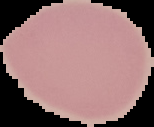
From a thin blood smear. Image is 154×127 pixels. Result: negative for malaria parasites. Cell region segmented out of the field of view; the surrounding area is masked to black.